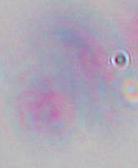 Toxoplasma gondii is shown. Captured at 1000x magnification. Micrograph.